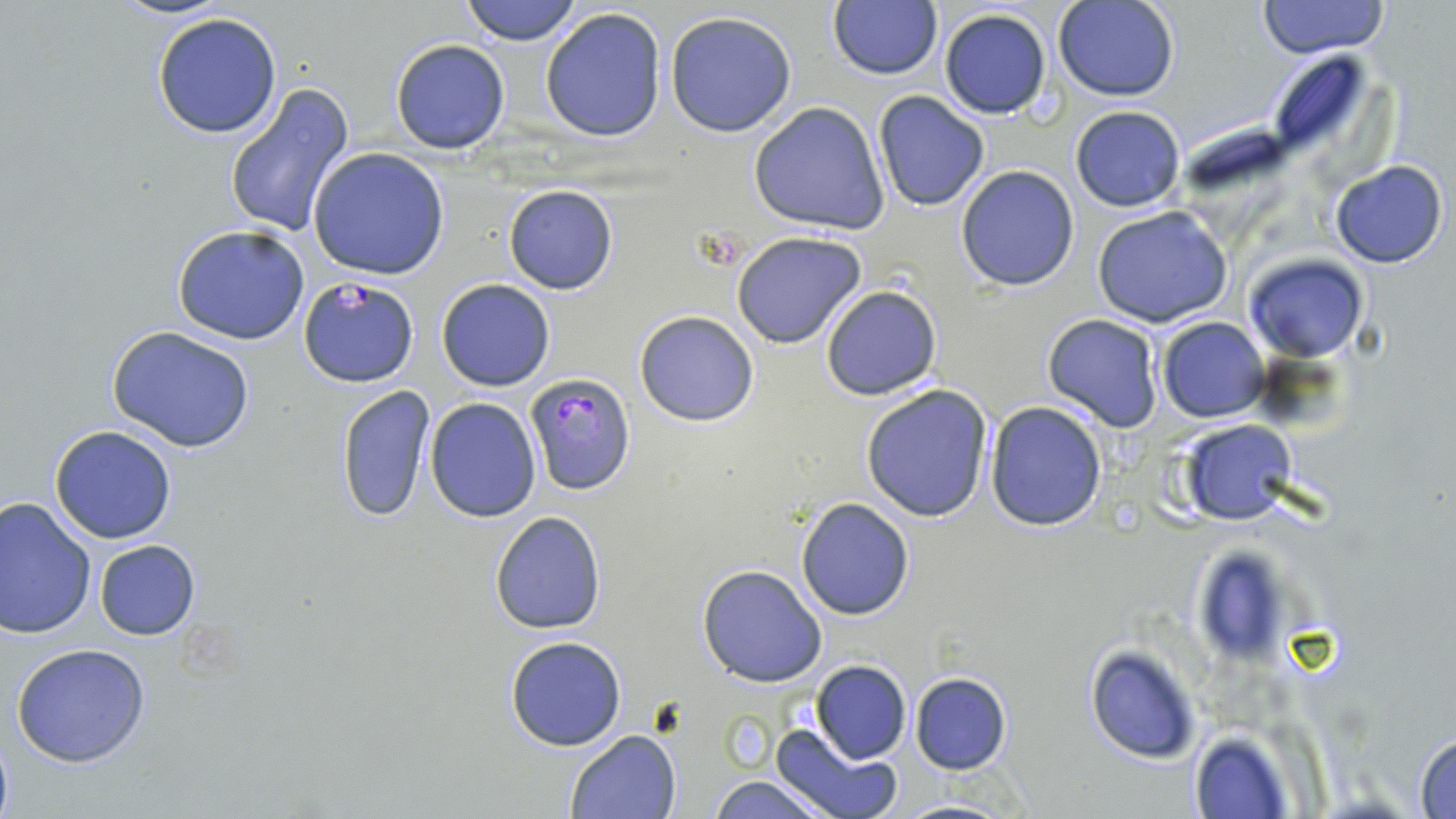

Summary:
  - Coordinate format: approximate bounding boxes as (x1,y1)-(x2,y2) corner pairs in pixels
  - Plasmodium falciparum-infected red blood cell locations: (299,276)-(417,387), (523,374)-(635,497)
  - Uninfected red blood cell locations: (110,0)-(232,21), (458,0)-(584,45), (1054,0)-(1179,101), (1258,0)-(1386,57), (826,1)-(942,80), (540,7)-(668,143), (937,8)-(1053,120), (664,9)-(798,139), (151,11)-(284,139), (389,39)-(511,154), (1263,49)-(1381,168), (223,84)-(355,238), (872,92)-(991,211), (749,101)-(890,236), (1070,105)-(1187,212), (308,148)-(450,280), (1328,160)-(1449,269), (954,164)-(1080,291), (503,185)-(618,295), (1093,206)-(1234,329), (172,224)-(311,345), (731,231)-(868,350), (1245,253)-(1367,362), (436,279)-(556,391), (820,283)-(943,401), (635,310)-(759,427), (1041,314)-(1164,433), (1156,317)-(1269,422), (107,326)-(257,452), (335,383)-(435,524), (860,384)-(993,523), (425,399)-(540,521), (986,402)-(1108,532), (1180,420)-(1296,526), (49,425)-(177,544), (0,496)-(97,638), (796,497)-(915,620), (489,511)-(606,635), (94,539)-(201,639), (1188,543)-(1303,667), (696,564)-(827,687), (504,637)-(628,751), (9,642)-(155,768), (1084,644)-(1203,764), (811,660)-(911,764), (909,673)-(1011,775), (769,724)-(900,819), (565,729)-(682,818), (1188,729)-(1297,818), (1412,732)-(1456,818), (707,774)-(835,818), (890,797)-(1021,818)
  - Slide-level diagnosis: Plasmodium falciparum
  - Preparation: thin blood smear
  - Field of view: one of a larger specimen
  - Magnification: 1000x
  - Image size: 1456×819 pixels
  - Stain: May-Grünwald-Giemsa
  - Modality: optical microscopy